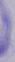

Summary:
  - Identification: trypanosome
  - Modality: micrograph
  - Magnification: 1000x